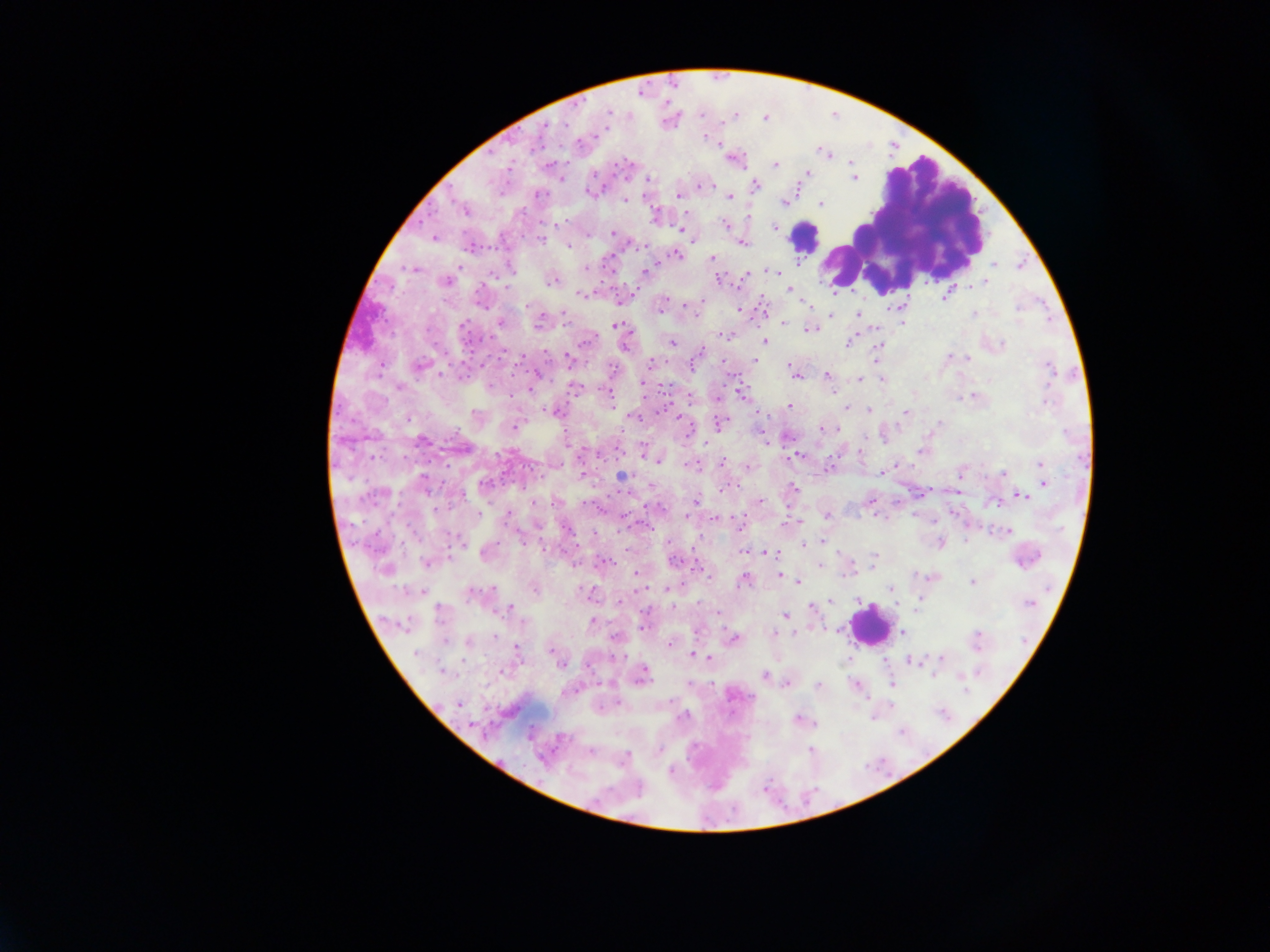
Approximate centers as x y in pixels. Plasmodium parasite locations: 607 112; 765 117; 704 137; 717 145; 824 151; 734 159; 850 162; 774 163; 807 173; 853 178; 647 179; 704 185; 753 185; 588 192; 538 194; 679 194; 729 197; 624 200; 781 201; 821 202; 464 210; 655 217; 748 217; 725 225; 774 227; 681 229; 612 233; 433 237; 542 239; 741 242; 569 245; 675 254; 711 259; 994 265; 585 267; 413 268; 772 270; 648 271; 744 276; 720 279; 446 281; 551 281; 986 281; 788 289; 947 292; 581 294; 481 297; 620 300; 806 302; 691 305; 901 305; 661 306; 888 308; 762 309; 739 310; 972 313; 858 314; 830 315; 901 321; 500 322; 539 322; 783 323; 615 326; 810 329; 875 330; 726 334; 764 341; 849 341; 671 343; 1001 345; 623 346; 878 347; 546 353; 521 356; 948 356; 967 359; 568 360; 755 361; 651 362; 723 363; 789 364; 420 366; 537 374; 797 375; 826 375; 860 379; 882 379; 642 383; 399 386; 575 387; 530 389; 608 393; 740 393; 972 395; 689 396; 717 399; 789 407; 845 407; 869 410; 554 411; 904 412; 678 416; 633 417; 408 419; 720 423; 939 425; 515 427; 821 429; 837 430; 421 441; 765 441; 704 443; 922 451; 644 452; 796 455; 659 460; 722 461; 1041 463; 691 465; 747 466; 827 468; 882 471; 1003 472; 1041 472; 622 476; 1044 483; 652 486; 424 488; 725 488; 793 488; 921 493; 1022 496; 695 501; 759 501; 534 502; 868 502; 996 502; 648 506; 508 515; 826 516; 685 517; 715 518; 799 522; 740 525; 566 528; 1008 530; 520 537; 822 542; 940 542; 804 544; 745 551; 767 551; 485 552; 674 561; 427 562; 602 563; 575 565; 697 566; 820 566; 873 566; 385 568; 636 574; 780 576; 933 576; 744 578; 797 582; 971 582; 639 587; 533 588; 667 589; 892 589; 422 592; 474 593; 589 594; 857 599; 920 599; 830 600; 620 601; 672 607; 812 607; 510 609; 440 611; 718 614; 785 616; 592 622; 404 624; 641 628; 837 629; 901 631; 773 633; 615 637; 732 638; 468 642; 669 644; 515 649; 551 649; 417 654; 695 655; 709 658; 941 658; 911 661; 560 662; 505 670; 642 674; 764 676; 786 683; 892 684; 818 685; 856 686; 458 704; 799 719; 810 749; 590 751; 659 751; 623 758. Leukocyte locations: 804 236; 868 625. Image is 1270×952 pixels. Single field of view. Thick blood film. Sample from Ghana. Mobile-phone photograph taken through the microscope.